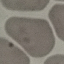

Summary:
  - Result: no malaria parasites detected
  - Image type: automatically extracted cell patch, resized to 64 × 64 pixels
  - Preparation: thin smear
  - Capture: smartphone camera at the microscope eyepiece
  - Stain: Giemsa